Point out Plasmodium parasites and leukocytes.
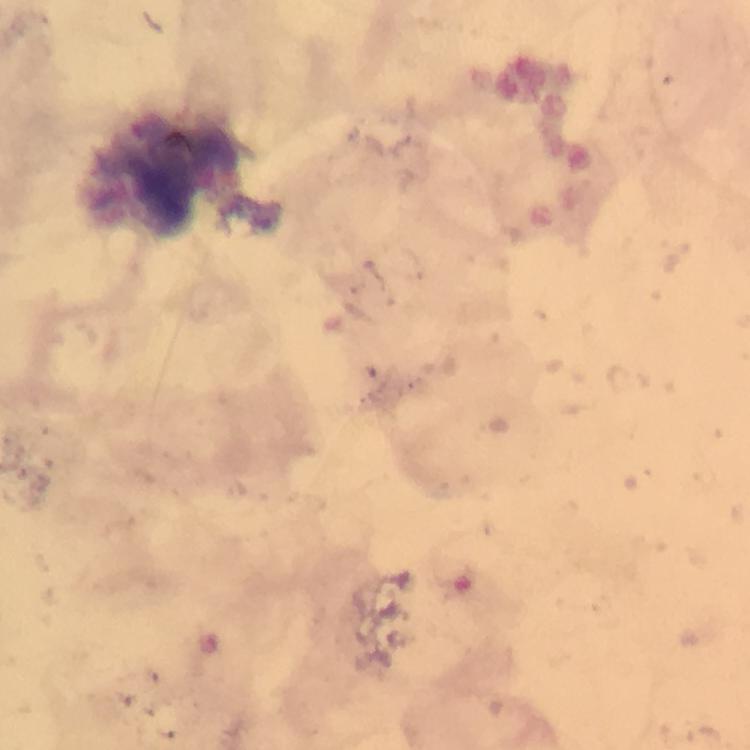
No Plasmodium parasites detected.
Approximate centers as [x, y] in pixels.
Leukocytes: [170, 176].

immersion oil = applied
image size = 750×750 pixels
capture = smartphone camera through the microscope
context = from a diagnostic examination for malaria
preparation = thick blood film
stain = Giemsa
cropped from = one field of view
magnification = 100x